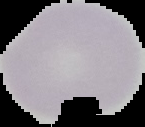
image_size: 145×127 pixels
image_type: segmented cell region with the area outside set to black
preparation: thin blood smear
malaria_status: uninfected